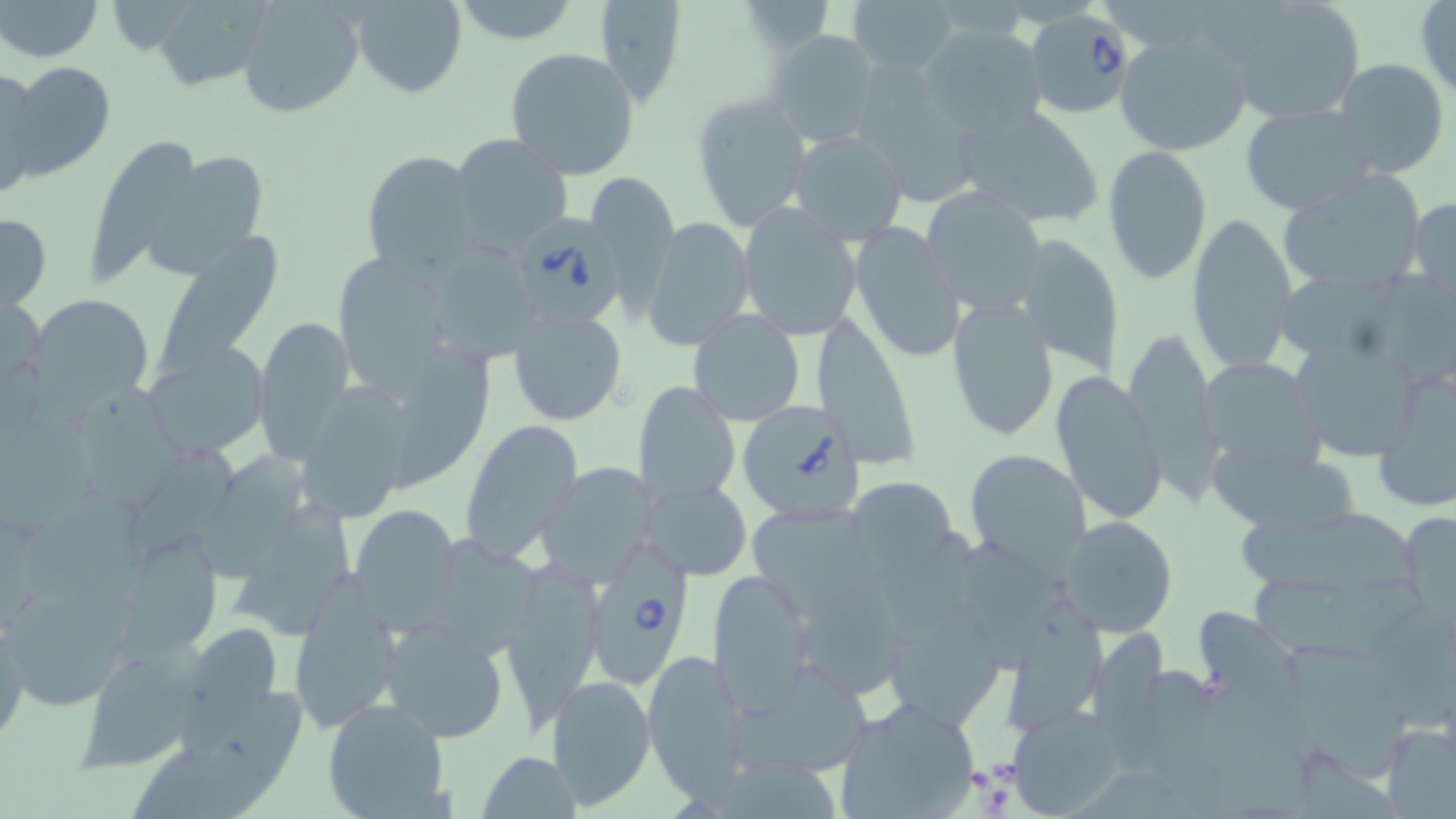
Summary:
  - Coordinate format: approximate bounding boxes as [x1, y1, x2, y2] in pixels
  - Babesia divergens-infected red blood cell locations: [1020, 11, 1136, 117], [515, 212, 631, 336], [739, 398, 870, 520], [587, 545, 698, 686]
  - Uninfected red blood cell locations: [1, 0, 104, 62], [350, 0, 467, 97], [450, 0, 583, 46], [593, 0, 687, 106], [737, 0, 835, 53], [849, 0, 961, 79], [1226, 0, 1369, 123], [1415, 0, 1456, 100], [154, 1, 274, 93], [236, 1, 363, 118], [920, 24, 1049, 137], [766, 29, 882, 151], [1116, 30, 1252, 158], [504, 47, 640, 180], [1331, 57, 1450, 179], [4, 61, 117, 182], [0, 65, 40, 198], [691, 93, 812, 232], [951, 101, 1105, 227], [1240, 103, 1373, 216], [787, 130, 909, 244], [91, 133, 207, 283], [448, 133, 574, 254], [1101, 145, 1213, 285], [128, 146, 271, 274], [358, 150, 482, 276], [1279, 169, 1429, 293], [583, 170, 680, 313], [922, 184, 1051, 314], [1409, 197, 1456, 288], [737, 203, 862, 340], [1187, 212, 1298, 375], [0, 213, 51, 313], [641, 217, 754, 351], [850, 221, 966, 365], [146, 229, 292, 386], [1010, 234, 1125, 376], [338, 256, 453, 400], [29, 294, 152, 406], [947, 296, 1061, 443], [506, 307, 629, 427], [687, 308, 808, 426], [809, 310, 921, 470], [254, 316, 358, 462], [1124, 327, 1218, 481], [1293, 332, 1426, 464], [393, 340, 500, 495], [145, 343, 268, 457], [1199, 359, 1327, 475], [1374, 365, 1456, 513], [1050, 369, 1166, 526], [632, 380, 741, 508], [305, 391, 414, 522], [460, 418, 586, 561], [125, 440, 255, 564], [1209, 446, 1374, 535], [964, 450, 1090, 571], [200, 454, 305, 589], [537, 463, 658, 586], [640, 476, 751, 581], [846, 476, 957, 575], [740, 502, 888, 618], [351, 504, 462, 631], [231, 506, 361, 645], [1241, 506, 1431, 594], [1401, 510, 1455, 621], [1059, 516, 1178, 636], [955, 546, 1079, 671], [500, 557, 607, 723], [707, 569, 819, 713], [1247, 569, 1427, 666], [286, 584, 404, 733], [6, 589, 145, 716], [804, 589, 906, 696], [876, 591, 1006, 731], [1009, 605, 1115, 736], [1191, 607, 1303, 705], [380, 619, 509, 741], [1, 620, 30, 747], [185, 622, 286, 718], [1284, 648, 1414, 787], [642, 649, 755, 806], [78, 651, 197, 769], [733, 666, 873, 777], [547, 676, 657, 809], [190, 693, 307, 811], [832, 696, 981, 819], [321, 699, 453, 819], [1009, 707, 1126, 815], [1382, 723, 1455, 818], [479, 750, 581, 819]
  - Slide-level diagnosis: Babesia divergens
  - Image size: 1456×819 pixels
  - Preparation: thin blood smear
  - Modality: light microscopy
  - Magnification: 1000x
  - Stain: May-Grünwald-Giemsa
  - Field of view: single